Report the malaria status of this cell.
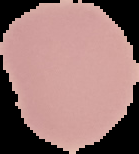
Uninfected.

Image is 139×154 pixels. From a thin blood smear. Segmented cell region on a black background.